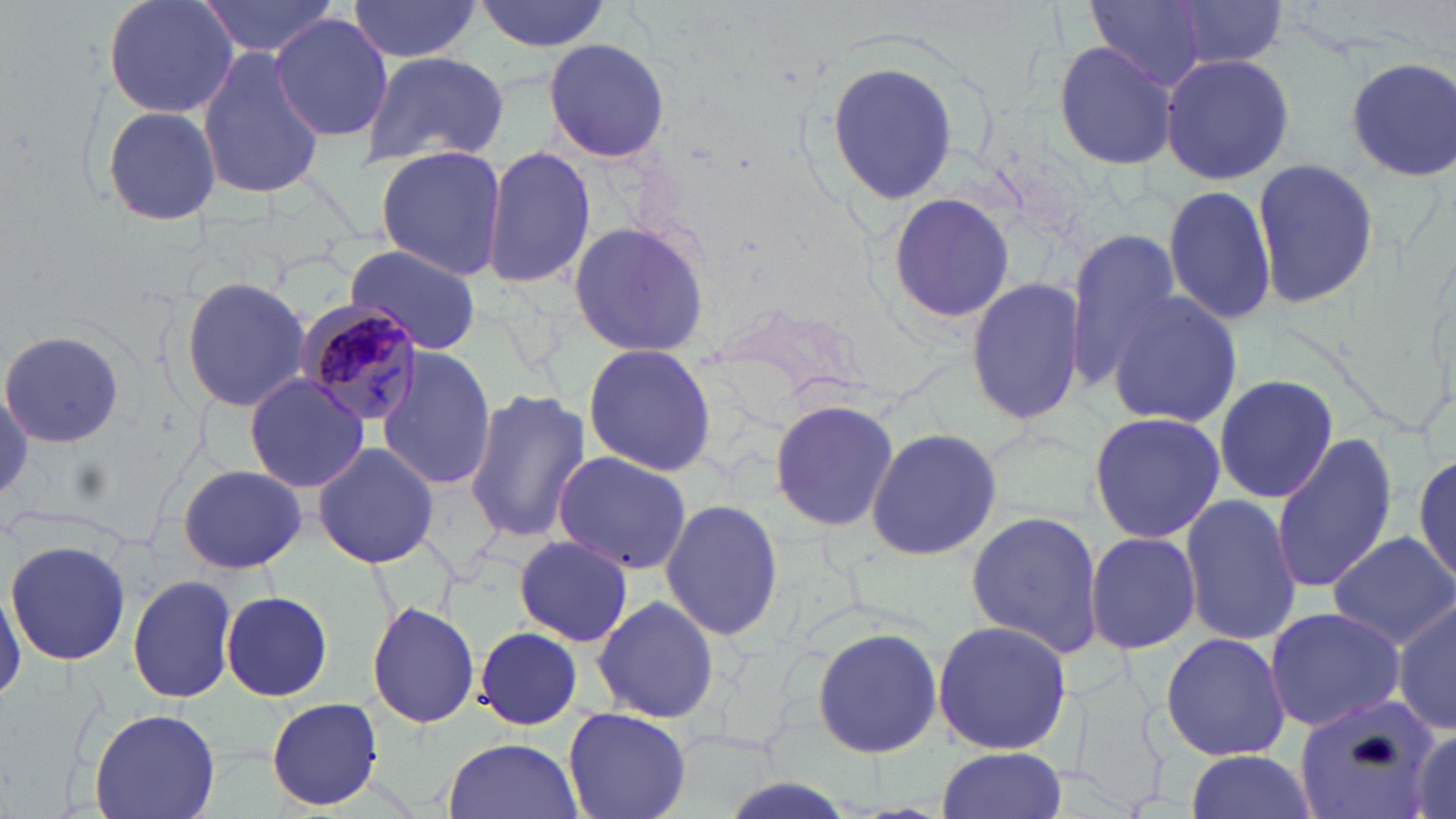

Approximate bounding boxes as named x1/y1/x2/y2 corners in pixels. Plasmodium malariae-infected red blood cell locations: (x1=297, y1=299, x2=426, y2=429). Uninfected red blood cell locations: (x1=101, y1=0, x2=242, y2=120), (x1=198, y1=0, x2=341, y2=60), (x1=471, y1=0, x2=613, y2=54), (x1=1085, y1=0, x2=1211, y2=85), (x1=1167, y1=0, x2=1289, y2=69), (x1=346, y1=2, x2=483, y2=61), (x1=271, y1=13, x2=394, y2=141), (x1=544, y1=36, x2=672, y2=165), (x1=1053, y1=40, x2=1181, y2=171), (x1=195, y1=42, x2=326, y2=203), (x1=360, y1=51, x2=510, y2=169), (x1=1161, y1=52, x2=1293, y2=185), (x1=1346, y1=57, x2=1456, y2=179), (x1=824, y1=58, x2=959, y2=208), (x1=97, y1=104, x2=226, y2=227), (x1=482, y1=145, x2=595, y2=290), (x1=374, y1=146, x2=508, y2=282), (x1=1249, y1=156, x2=1380, y2=307), (x1=1163, y1=183, x2=1277, y2=325), (x1=885, y1=191, x2=1019, y2=325), (x1=566, y1=220, x2=711, y2=359), (x1=1062, y1=228, x2=1180, y2=390), (x1=343, y1=247, x2=484, y2=352), (x1=966, y1=272, x2=1089, y2=428), (x1=181, y1=276, x2=311, y2=414), (x1=1103, y1=290, x2=1243, y2=432), (x1=2, y1=329, x2=125, y2=449), (x1=580, y1=343, x2=717, y2=475), (x1=374, y1=346, x2=497, y2=491), (x1=243, y1=374, x2=370, y2=494), (x1=1212, y1=374, x2=1339, y2=506), (x1=464, y1=388, x2=590, y2=543), (x1=767, y1=398, x2=901, y2=533), (x1=1087, y1=409, x2=1228, y2=545), (x1=864, y1=426, x2=1004, y2=561), (x1=1271, y1=433, x2=1399, y2=593), (x1=312, y1=442, x2=440, y2=570), (x1=551, y1=451, x2=693, y2=575), (x1=1413, y1=451, x2=1456, y2=593), (x1=178, y1=464, x2=306, y2=574), (x1=1179, y1=492, x2=1303, y2=646), (x1=661, y1=495, x2=784, y2=642), (x1=965, y1=510, x2=1105, y2=660), (x1=1086, y1=530, x2=1201, y2=654), (x1=1327, y1=533, x2=1456, y2=647), (x1=513, y1=536, x2=633, y2=646), (x1=5, y1=537, x2=132, y2=667), (x1=128, y1=574, x2=239, y2=703), (x1=1, y1=579, x2=24, y2=705), (x1=221, y1=590, x2=332, y2=702), (x1=592, y1=594, x2=721, y2=723), (x1=1393, y1=599, x2=1456, y2=737), (x1=368, y1=600, x2=480, y2=728), (x1=1263, y1=606, x2=1407, y2=732), (x1=931, y1=619, x2=1075, y2=756), (x1=475, y1=626, x2=584, y2=730), (x1=810, y1=626, x2=944, y2=760), (x1=1159, y1=632, x2=1291, y2=762), (x1=1296, y1=695, x2=1439, y2=819), (x1=265, y1=697, x2=385, y2=810), (x1=561, y1=705, x2=692, y2=819), (x1=89, y1=707, x2=220, y2=819), (x1=1407, y1=725, x2=1456, y2=819), (x1=442, y1=736, x2=585, y2=819), (x1=935, y1=747, x2=1068, y2=819), (x1=1182, y1=750, x2=1317, y2=818). Slide-level diagnosis: Plasmodium malariae. Image is 1456×819 pixels. Single field of view. May-Grünwald-Giemsa stain. Captured at 1000x magnification. Thin blood film. Optical microscopy.